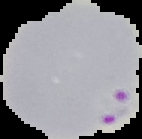

Image is 142×139 pixels. Malaria status: parasitized. Segmented cell region on a black background. From a thin blood film.